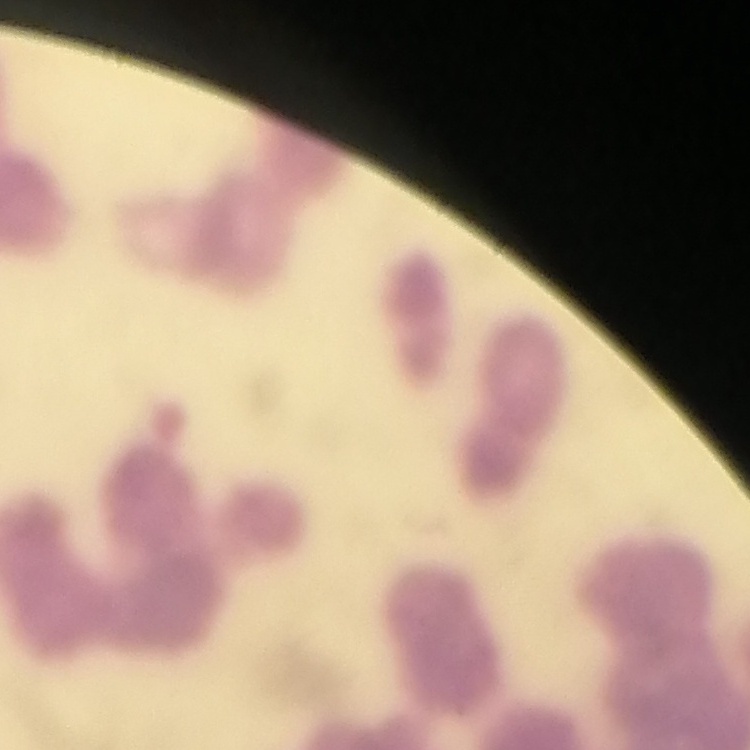

red blood cell morphology = rouleaux formation
preparation = thin blood smear
stain = Field's or Giemsa
image type = square crop of a larger photomicrograph